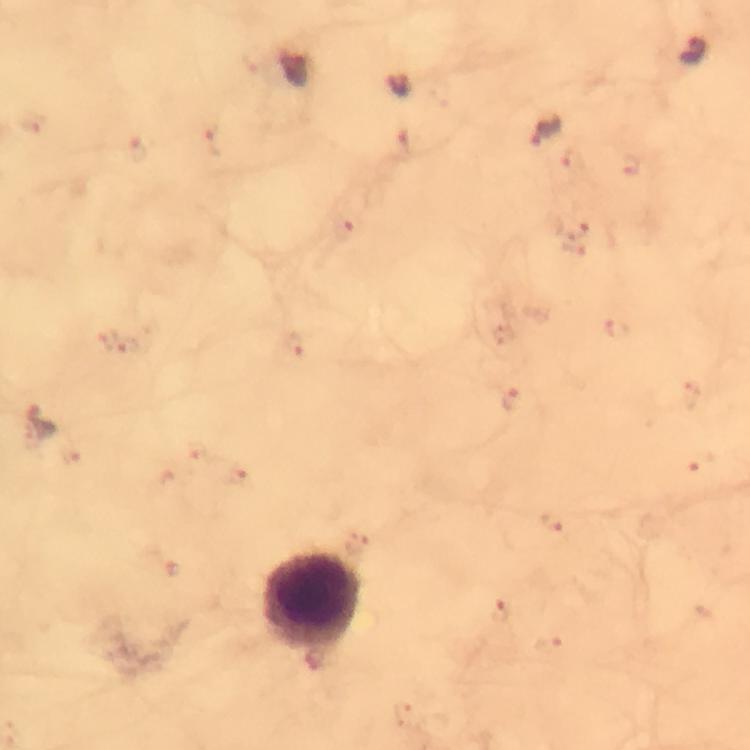 Approximate centers as {x, y} in pixels. Leukocyte locations: {311, 600}. Plasmodium parasite locations: {692, 51}, {294, 67}, {549, 131}, {215, 143}, {139, 152}, {628, 165}, {577, 229}, {344, 230}, {617, 328}, {118, 344}, {292, 344}, {509, 398}, {38, 423}, {555, 522}, {356, 547}, {497, 612}. From a malaria diagnostic workup. 100x magnification. Immersion oil was used. Thick blood film. Giemsa stain. A crop from one field of view. Photographed through the microscope with a smartphone camera. Image is 750×750 pixels.